Describe the morphology of the red blood cells.
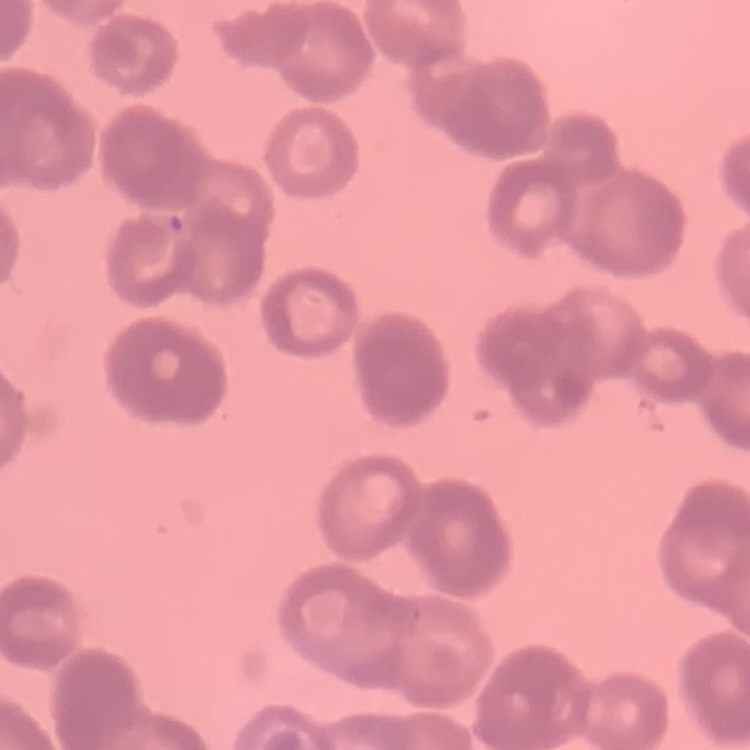
Rouleaux formation.

Thin peripheral smear. One tile cut from a larger photomicrograph. Field's or Giemsa stain.